Locate every malaria parasite.
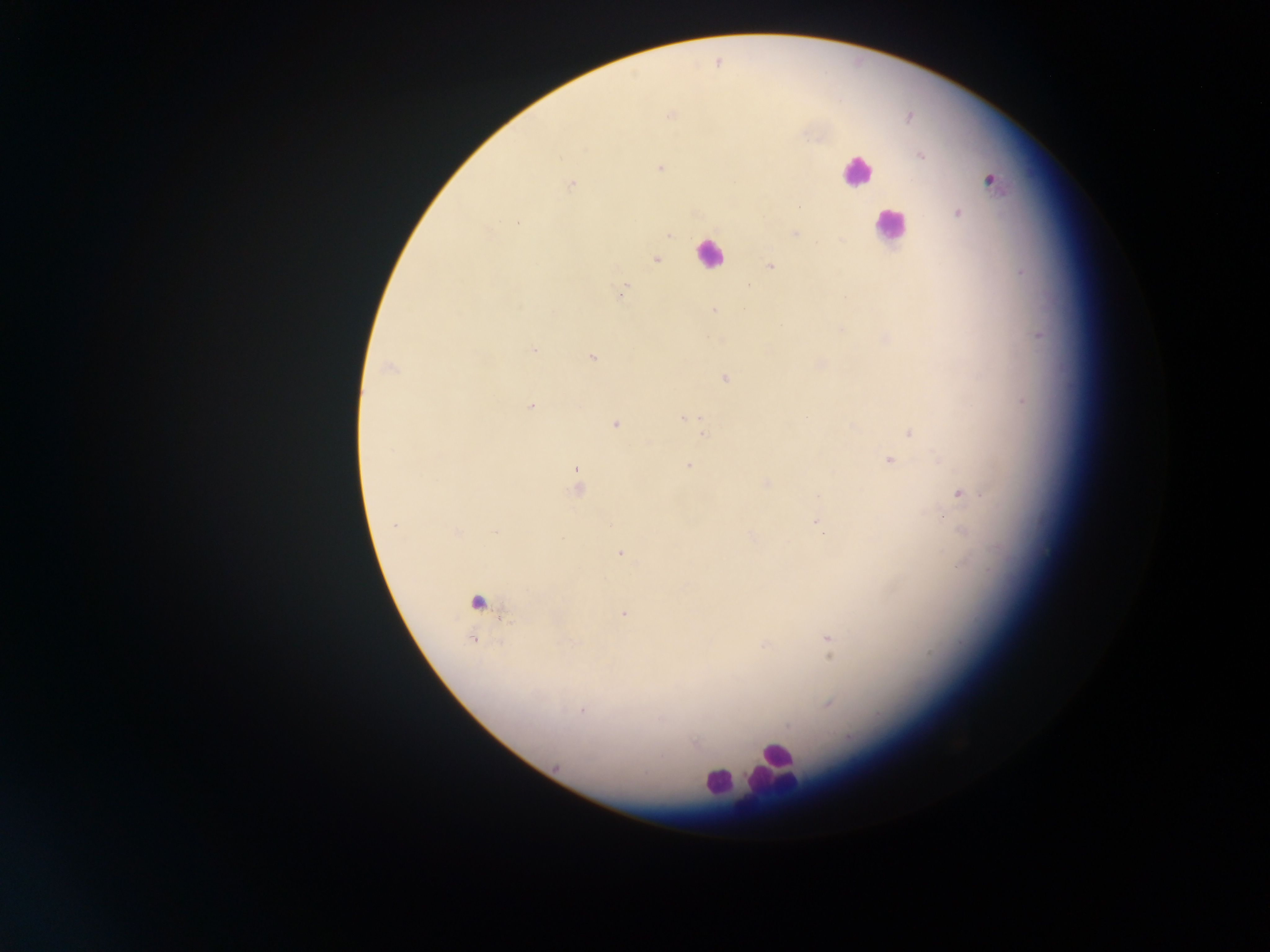
Approximate centers as [x, y] in pixels.
Malaria parasites: [717, 61], [670, 115], [920, 154], [660, 168], [989, 180], [570, 184], [956, 212], [518, 223], [794, 233], [670, 234], [655, 259], [770, 265], [622, 292], [715, 311], [1038, 334], [885, 340], [533, 349], [591, 358], [390, 368], [724, 377], [1022, 401], [531, 406], [685, 418], [614, 424], [704, 432], [910, 432], [889, 461], [689, 465], [766, 483], [578, 485], [959, 492], [942, 517], [816, 520], [751, 534], [620, 552], [477, 603], [623, 613], [828, 639], [473, 640], [765, 645], [828, 703].

leukocyte_locations: 'approximate centers as [x, y] in pixels: [856, 170], [890, 226], [710, 253], [775, 764], [717, 783]'
image_size: 1270×952 pixels
preparation: thick blood smear
capture: mobile-phone photograph through a microscope
country: Ghana
field_of_view: single